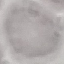
Result: negative for malaria parasites. Thin blood smear. Photographed with a smartphone camera at the microscope eyepiece. Giemsa-stained preparation. Cell patch, automatically extracted from a larger field of view and resized to 64 × 64 pixels.